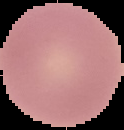
Summary:
  - Image type: cell region segmented out of the field of view; surrounding area masked to black
  - Malaria status: uninfected
  - Preparation: thin blood film
  - Image size: 124×130 pixels